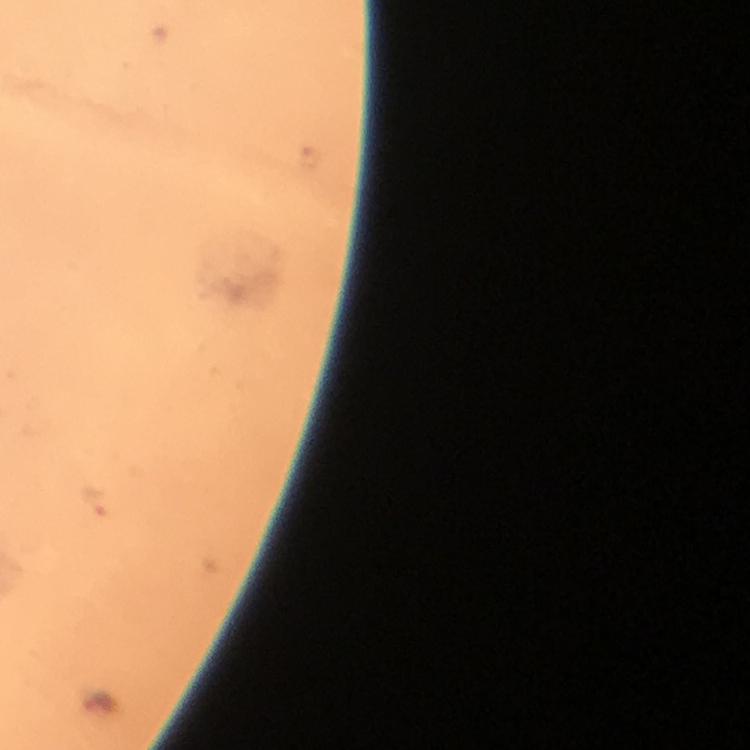

Approximate centers as [x, y] in pixels.
Summary:
  - Malaria parasite locations: [94, 503]
  - Preparation: thick blood film
  - Capture: smartphone camera through the microscope
  - Context: from a diagnostic examination for malaria
  - Immersion oil: applied
  - Magnification: 100x
  - Cropped from: one field of view
  - Stain: Giemsa
  - Image size: 750×750 pixels